Assess this cell for malaria.
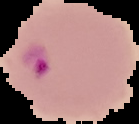

Parasitized.

image type = segmented cell region on a black background
image size = 139×124 pixels
preparation = thin blood film